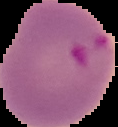
Summary:
  - Image type: segmented cell region on a black background
  - Preparation: thin blood film
  - Malaria status: parasitized
  - Image size: 118×127 pixels